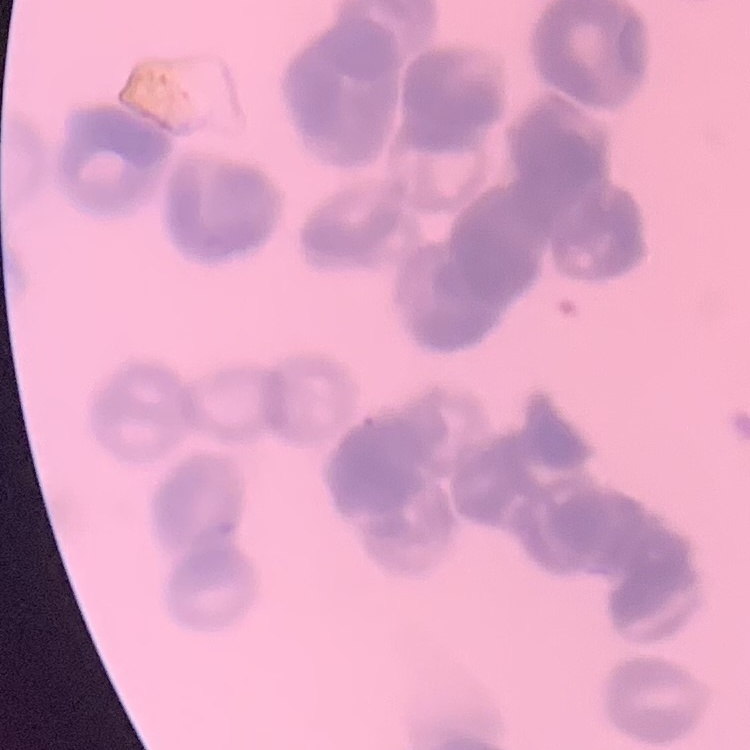
erythrocyte morphology = rouleaux formation
image type = square crop of a larger photomicrograph
preparation = thin peripheral smear
stain = Field's or Giemsa